Assess this cell for malaria.
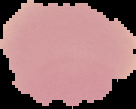

Uninfected.

preparation = thin blood smear
image size = 136×109 pixels
image type = cell region segmented out of the field of view; surrounding area masked to black